Classify this cell by malaria status.
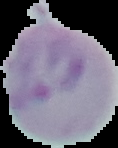

It is uninfected.

Segmented cell region on a black background. From a thin blood film. Image is 118×148 pixels.